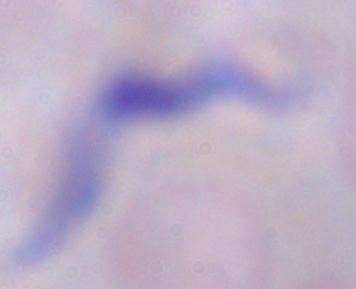
identification: trypanosome
modality: photomicrograph
magnification: 1000x